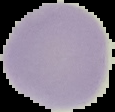

{
  "image_size": "115×112 pixels",
  "preparation": "thin blood smear",
  "image_type": "segmented cell region with the area outside set to black",
  "malaria_status": "uninfected"
}